Report the malaria status of this cell.
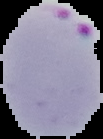
Parasitized.

Summary:
  - Image type: segmented cell region with the area outside set to black
  - Preparation: thin blood film
  - Image size: 103×139 pixels